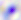
modality = photomicrograph
magnification = 400x
identification = Toxoplasma gondii